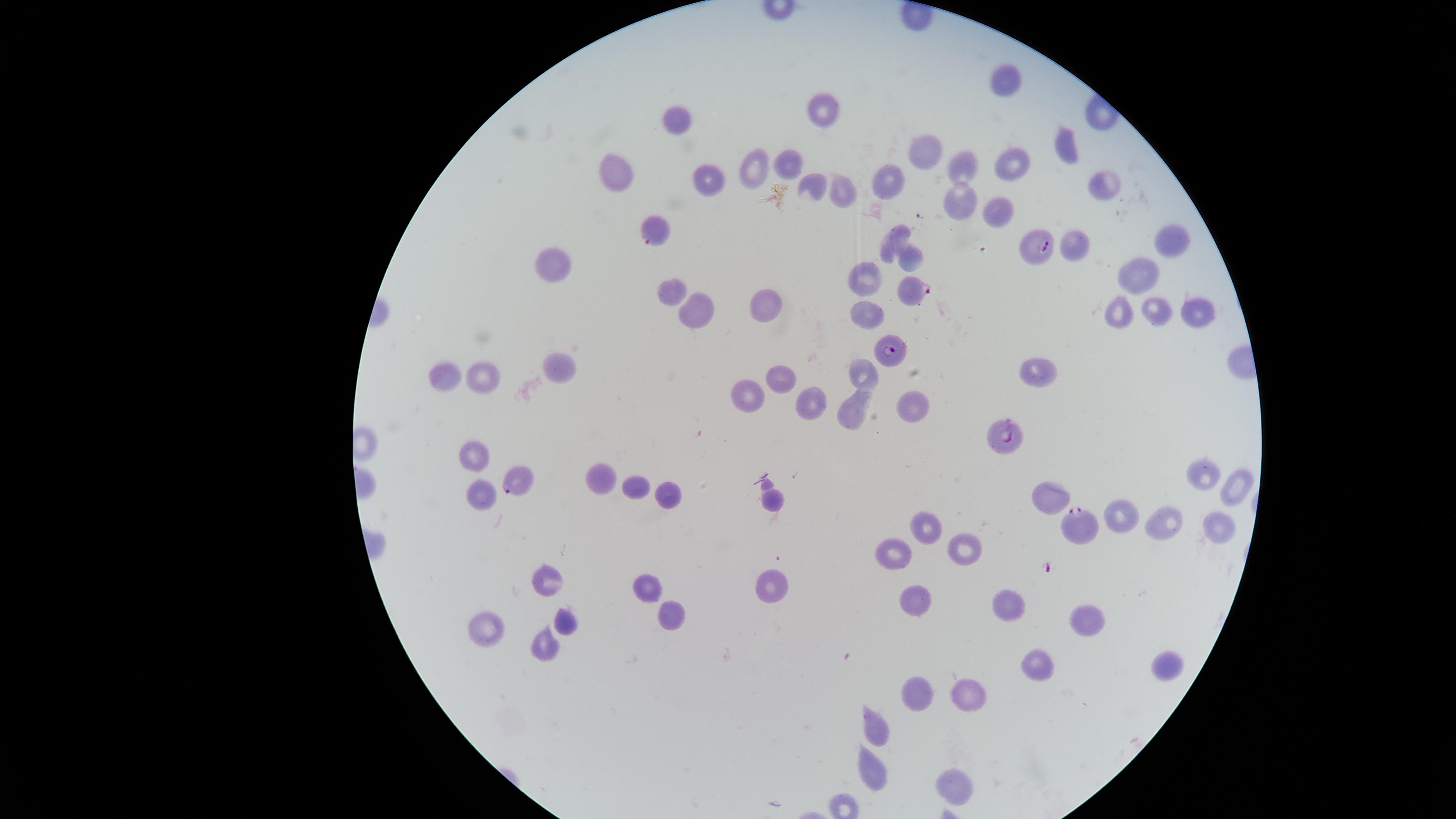
image_size: 1456×819 pixels
stain: Giemsa
parasitized_RBCs: 'approximate marker points as (x, y) in pixels: (656, 229), (1040, 245), (913, 290), (892, 350), (1007, 434), (518, 480), (1079, 524)'
preparation: thin blood smear
presence: malaria parasites seen
species: Plasmodium falciparum
field_of_view: single
visible_region: circular
capture: smartphone photograph through the microscope eyepiece
uninfected_RBCs: 'approximate marker points as (x, y) in pixels: (1005, 83), (824, 109), (675, 120), (1064, 149), (921, 151), (791, 162), (969, 166), (1011, 166), (756, 169), (616, 175), (707, 178), (817, 181), (883, 183), (842, 190), (960, 207), (999, 214), (893, 236), (1168, 239), (1075, 245), (907, 263), (551, 265), (1141, 272), (866, 277), (670, 288), (761, 304), (689, 309), (1120, 310), (873, 311), (1159, 312), (1194, 313), (559, 365), (868, 373), (482, 374), (442, 375), (1038, 375), (780, 376), (744, 393), (809, 400), (906, 405), (851, 409), (474, 459), (1199, 478), (603, 481), (640, 486), (1236, 488), (481, 494), (1046, 494), (669, 495), (771, 499), (1122, 518), (1159, 521), (925, 527), (1214, 533), (959, 544), (894, 557), (546, 584), (648, 585), (773, 590), (915, 601), (1007, 605), (1082, 616), (673, 618), (563, 621), (485, 625), (545, 644), (1166, 663), (1033, 664), (922, 693), (968, 697), (879, 730), (867, 765), (944, 789)'